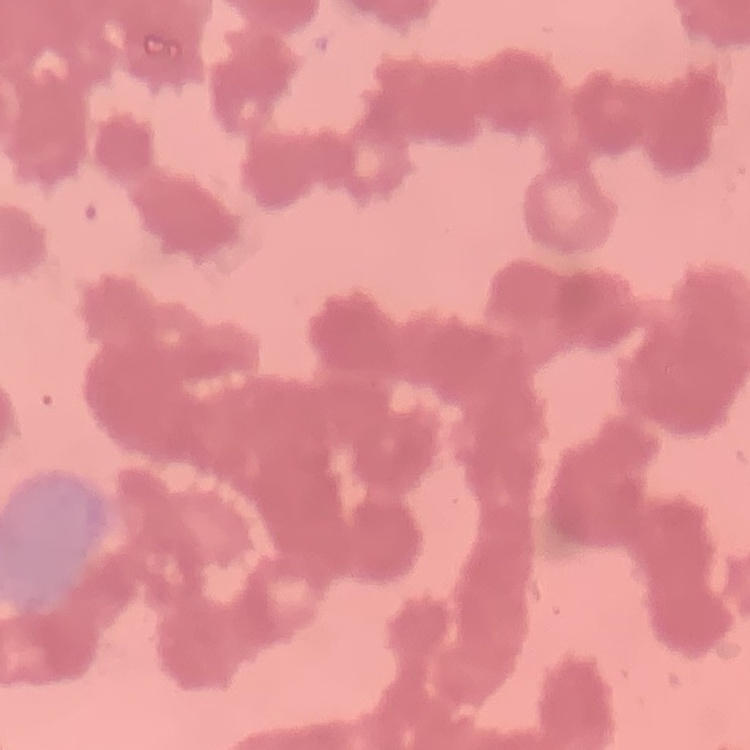
Summary:
  - Erythrocyte morphology: rouleaux formation
  - Stain: Field's or Giemsa
  - Preparation: thin peripheral smear
  - Image type: square crop of a larger photomicrograph